Report the malaria status of this cell.
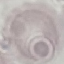
Uninfected.

{
  "stain": "Giemsa",
  "preparation": "thin blood film",
  "capture": "smartphone camera at the microscope eyepiece",
  "image_type": "cell patch, automatically extracted from a larger field of view and resized to 64 × 64 pixels"
}